Outline each white blood cell.
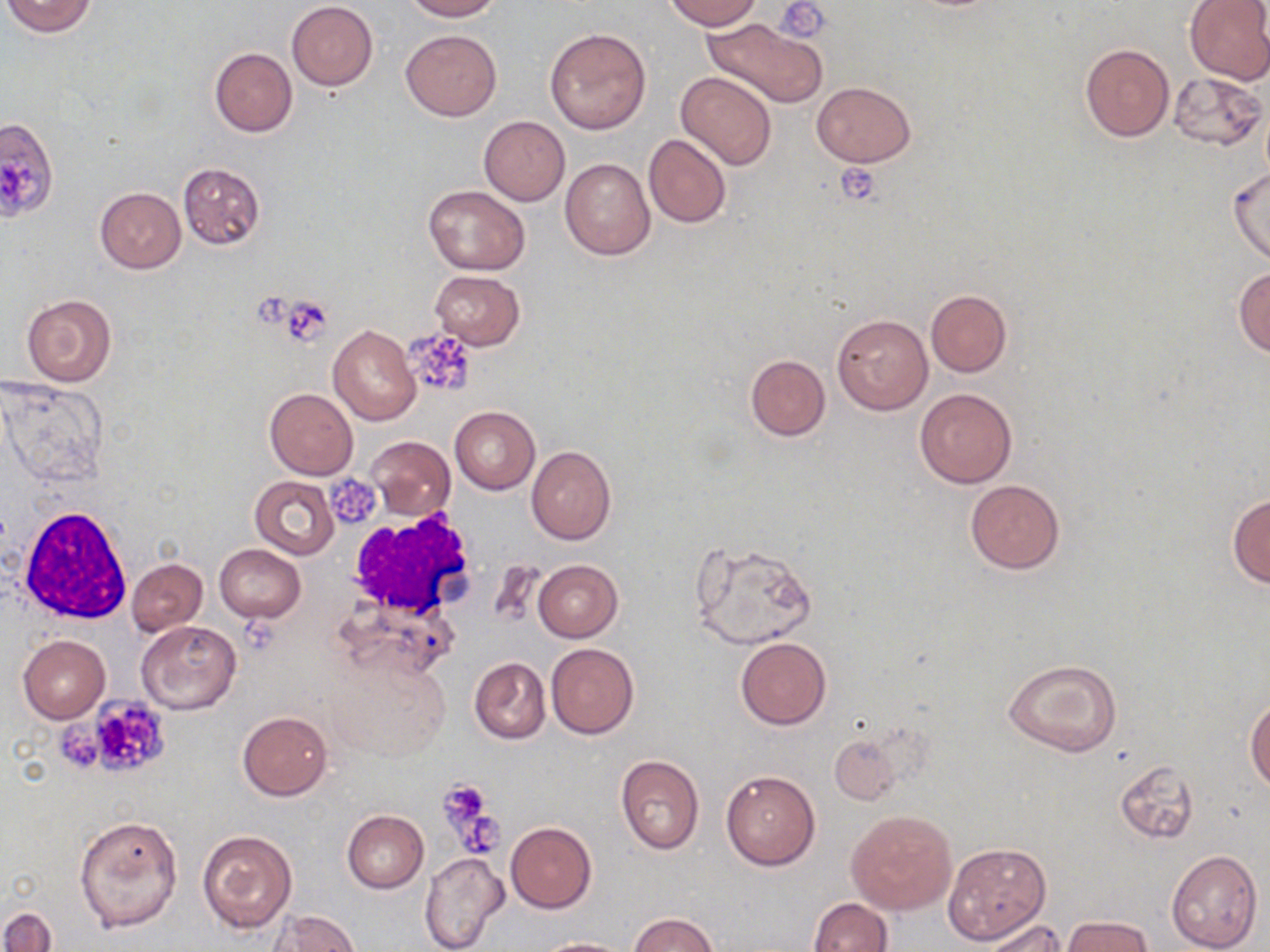

Approximate bounding boxes as (x1,y1)-(x2,y2) corner pairs in pixels.
White blood cells: (18,504)-(134,625), (346,512)-(480,619).

slide-level diagnosis = negative for blood parasites
image size = 1270×952 pixels
field of view = one of a larger specimen
magnification = 1000x
platelet locations = approximate bounding boxes as (x1,y1)-(x2,y2) corner pairs in pixels: (775,1)-(832,43), (0,156)-(39,201), (835,162)-(883,207), (278,296)-(332,345), (403,328)-(480,399), (330,474)-(379,525), (237,619)-(285,654), (66,695)-(172,781), (439,779)-(493,829), (457,819)-(505,853)
uninfected red blood cell locations = approximate bounding boxes as (x1,y1)-(x2,y2) corner pairs in pixels: (1,0)-(98,38), (401,0)-(502,21), (663,0)-(762,31), (1184,0)-(1270,86), (286,1)-(378,90), (700,18)-(827,108), (544,27)-(651,134), (400,28)-(502,121), (1079,45)-(1174,141), (208,47)-(298,137), (675,71)-(778,171), (1167,72)-(1266,152), (812,81)-(915,166), (479,116)-(569,205), (0,118)-(58,225), (643,133)-(731,228), (560,158)-(654,260), (178,162)-(265,249), (1229,165)-(1270,266), (424,184)-(530,275), (95,187)-(185,273), (1234,267)-(1270,357), (430,270)-(526,349), (925,289)-(1012,376), (21,294)-(117,386), (832,313)-(933,414), (328,325)-(420,425), (745,354)-(830,441), (1,380)-(105,484), (265,388)-(358,479), (915,388)-(1016,488), (450,405)-(540,494), (366,436)-(454,519), (526,446)-(616,545), (250,475)-(339,560), (964,479)-(1065,574), (1227,493)-(1270,588), (692,539)-(819,650), (215,544)-(305,622), (126,558)-(207,637), (533,559)-(623,641), (136,622)-(241,714), (19,635)-(110,722), (736,636)-(830,729), (546,643)-(638,739), (327,649)-(457,766), (469,657)-(550,744), (1003,658)-(1122,758), (1245,696)-(1270,791), (237,712)-(332,801), (829,731)-(902,806), (615,754)-(705,854), (1114,759)-(1200,846), (720,769)-(820,870), (846,807)-(957,916), (342,811)-(428,893), (73,814)-(183,933), (506,821)-(596,913), (197,829)-(297,933), (944,843)-(1049,944), (1166,849)-(1264,951), (419,852)-(509,952), (807,899)-(893,952), (2,907)-(56,952), (270,912)-(360,952), (627,913)-(720,952), (1062,916)-(1154,952), (982,918)-(1070,951), (532,937)-(631,952)
stain = May-Grünwald-Giemsa
preparation = thin blood film
modality = light microscopy